State which parasite is depicted.
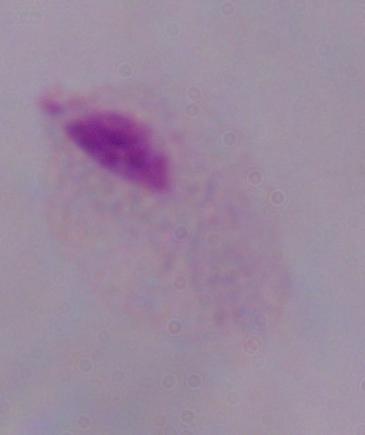

A trichomonad.

Micrograph. Captured at 1000x magnification.